Outline each blood parasite and name the species.
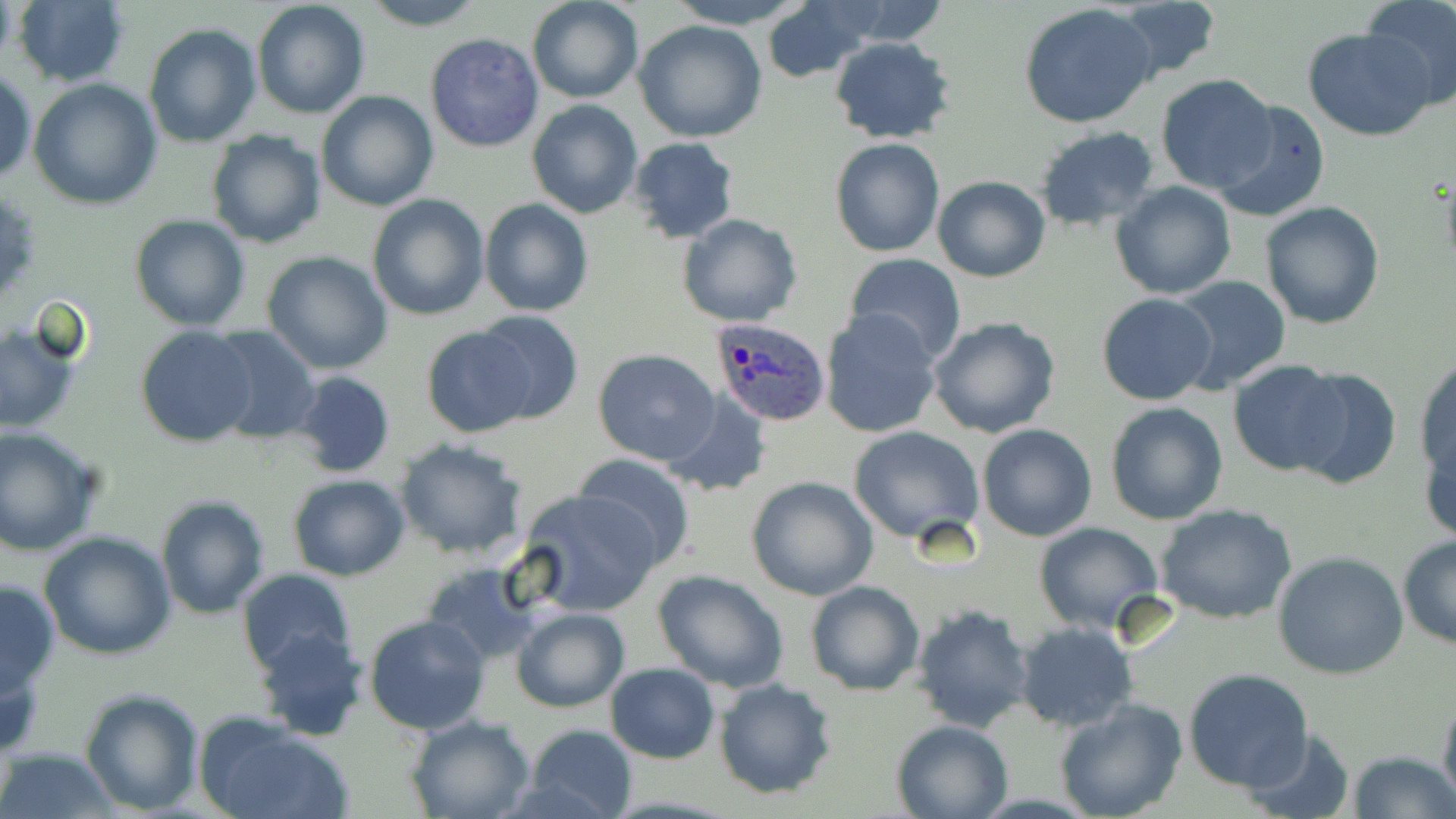
Approximate bounding boxes as (x1, y1, x2, y2) in pixels.
Plasmodium ovale-infected red blood cells: (709, 318, 831, 427).
No Plasmodium falciparum, Plasmodium malariae, Plasmodium vivax, Babesia divergens, or Trypanosoma brucei observed.

Uninfected red blood cell locations: (251, 0, 371, 120), (358, 0, 489, 30), (527, 0, 643, 104), (664, 0, 811, 28), (1362, 0, 1456, 110), (13, 1, 130, 87), (764, 3, 874, 82), (1116, 3, 1222, 81), (1019, 4, 1159, 130), (632, 19, 769, 143), (144, 23, 261, 147), (1302, 26, 1435, 141), (424, 32, 544, 154), (830, 37, 956, 145), (1, 67, 36, 186), (1154, 72, 1277, 195), (29, 77, 162, 210), (315, 91, 438, 211), (527, 100, 642, 219), (1211, 100, 1332, 223), (1034, 125, 1161, 232), (205, 130, 327, 247), (627, 136, 740, 244), (830, 137, 944, 256), (933, 176, 1050, 282), (1110, 182, 1237, 298), (365, 193, 489, 320), (479, 198, 593, 317), (1261, 201, 1386, 329), (129, 213, 251, 331), (677, 213, 802, 327), (263, 252, 393, 374), (844, 254, 967, 364), (1166, 274, 1292, 395), (1097, 293, 1217, 405), (820, 308, 942, 438), (473, 309, 584, 424), (927, 316, 1061, 439), (0, 320, 81, 435), (418, 323, 537, 438), (135, 326, 258, 447), (209, 328, 322, 443), (592, 347, 721, 465), (1414, 356, 1455, 488), (1228, 361, 1349, 475), (1286, 367, 1402, 492), (291, 371, 397, 477), (661, 392, 772, 497), (1104, 401, 1229, 525), (977, 423, 1097, 541), (1421, 423, 1456, 549), (0, 425, 104, 555), (848, 426, 984, 545), (393, 438, 528, 561), (574, 453, 696, 569), (288, 474, 412, 581), (746, 475, 879, 601), (516, 488, 664, 617), (155, 495, 271, 619), (1155, 505, 1298, 624), (1033, 522, 1163, 634), (39, 531, 177, 660), (1398, 536, 1456, 650), (1273, 552, 1409, 679), (420, 558, 541, 665), (237, 568, 357, 678), (648, 568, 791, 694), (0, 578, 60, 697), (806, 581, 926, 697), (910, 603, 1036, 733), (511, 608, 629, 712), (363, 614, 492, 735), (1015, 623, 1138, 732), (254, 628, 368, 741), (0, 648, 48, 762), (605, 663, 720, 763), (1182, 667, 1315, 792), (713, 677, 839, 799), (79, 685, 205, 814), (1437, 687, 1456, 817), (1053, 698, 1189, 819), (403, 715, 535, 819), (195, 716, 349, 819), (890, 718, 1014, 819), (521, 722, 639, 819), (1240, 728, 1356, 816), (0, 748, 118, 817), (1347, 750, 1456, 819). Slide-level diagnosis: Plasmodium ovale. Optical microscopy. May-Grünwald-Giemsa-stained preparation. Image is 1456×819 pixels. One field of a larger specimen. Thin blood smear. 1000x magnification.